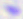
Summary:
  - Magnification: 400x
  - Modality: photomicrograph
  - Identification: Toxoplasma gondii